Outline each Trypanosoma brucei.
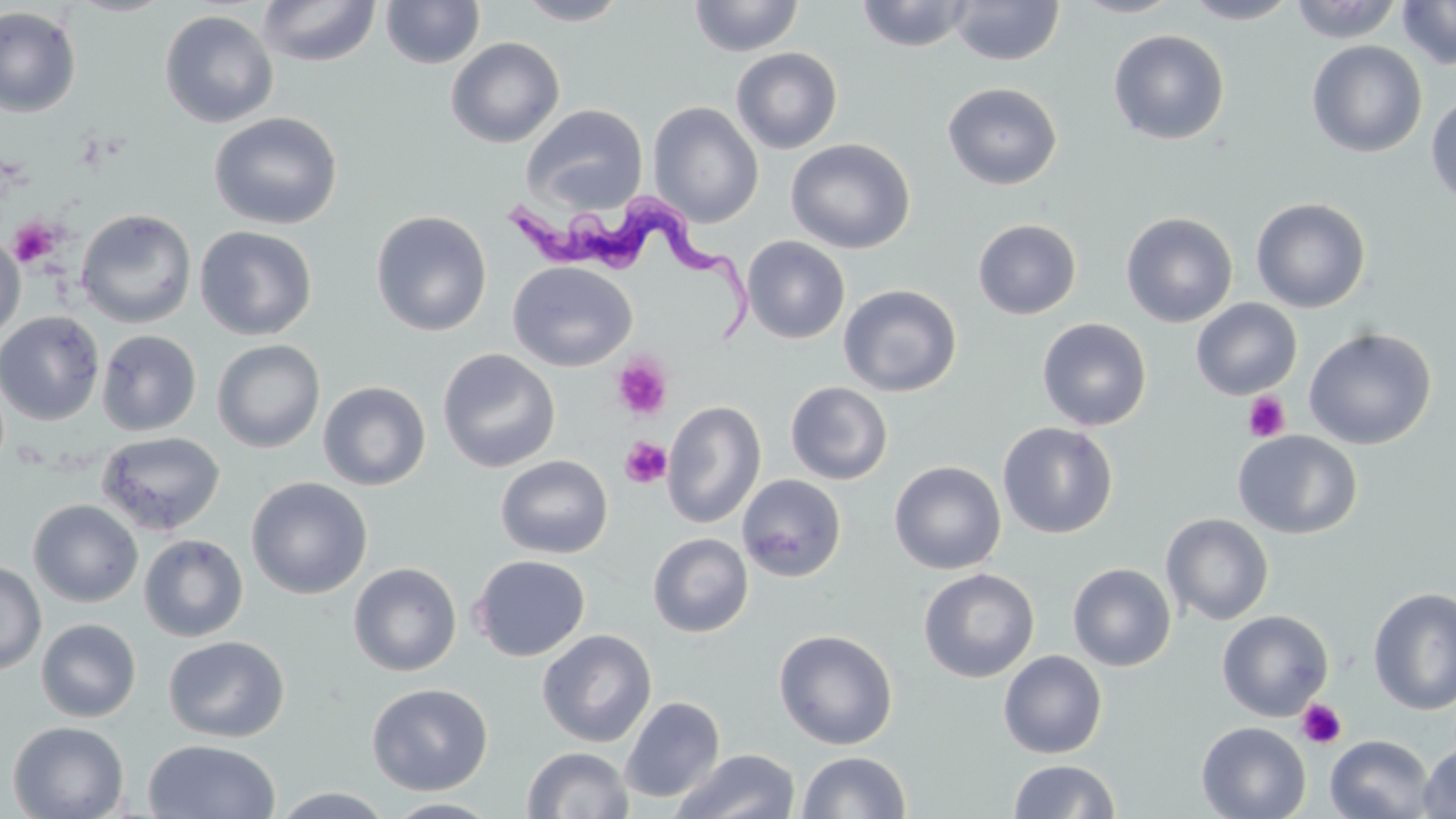
Approximate bounding boxes as (x1,y1)-(x2,y2) corner pairs in pixels.
Trypanosoma brucei: (509,192)-(756,345).

slide_level_diagnosis: Trypanosoma brucei
magnification: 1000x
field_of_view: one of a larger specimen
uninfected_red_blood_cell_locations: 'approximate bounding boxes as (x1,y1)-(x2,y2) corner pairs in pixels: (68,0)-(176,17), (256,0)-(381,68), (380,0)-(486,69), (688,0)-(804,57), (1070,0)-(1183,18), (1183,0)-(1299,24), (1289,0)-(1402,43), (515,1)-(630,25), (854,1)-(976,52), (948,1)-(1065,66), (1396,1)-(1456,70), (0,6)-(82,117), (159,9)-(278,128), (1108,29)-(1230,145), (445,37)-(565,148), (1306,40)-(1427,158), (731,47)-(843,154), (942,82)-(1062,190), (1426,91)-(1456,209), (647,101)-(764,227), (521,104)-(648,214), (208,112)-(343,230), (785,138)-(916,255), (1250,196)-(1372,313), (75,209)-(197,329), (371,210)-(492,336), (1120,212)-(1239,327), (972,218)-(1082,320), (194,225)-(317,340), (0,233)-(26,342), (742,236)-(850,344), (507,261)-(637,371), (838,284)-(962,397), (1190,299)-(1302,400), (0,310)-(105,425), (1036,317)-(1152,431), (1303,327)-(1437,449), (97,329)-(202,436), (211,339)-(325,453), (437,348)-(560,473), (317,381)-(431,490), (785,381)-(893,485), (661,400)-(766,529), (997,421)-(1119,539), (1233,430)-(1363,539), (96,431)-(226,536), (495,455)-(614,559), (888,460)-(1006,574), (736,474)-(847,582), (245,476)-(373,599), (28,499)-(143,607), (1161,513)-(1275,625), (139,533)-(248,642), (648,533)-(753,637), (470,554)-(591,661), (0,560)-(46,674), (348,562)-(462,676), (1067,563)-(1176,671), (918,568)-(1040,682), (1367,586)-(1456,715), (1217,610)-(1334,721), (36,618)-(141,722), (773,628)-(898,750), (537,629)-(657,747), (163,634)-(290,742), (998,650)-(1107,759), (366,682)-(493,795), (619,696)-(725,803), (7,721)-(129,819), (1196,722)-(1311,819), (1325,734)-(1435,818), (143,739)-(281,819), (1418,741)-(1456,818), (522,746)-(634,819), (670,748)-(800,819), (796,750)-(911,818), (1008,759)-(1119,817), (269,787)-(397,818), (382,798)-(505,818)'
platelet_locations: 'approximate bounding boxes as (x1,y1)-(x2,y2) corner pairs in pixels: (9,217)-(62,267), (612,356)-(672,421), (1243,392)-(1291,442), (619,436)-(672,489), (1296,699)-(1347,750)'
stain: May-Grünwald-Giemsa
preparation: thin blood film
image_size: 1456×819 pixels
modality: light microscopy